Comment on the morphology of the erythrocytes.
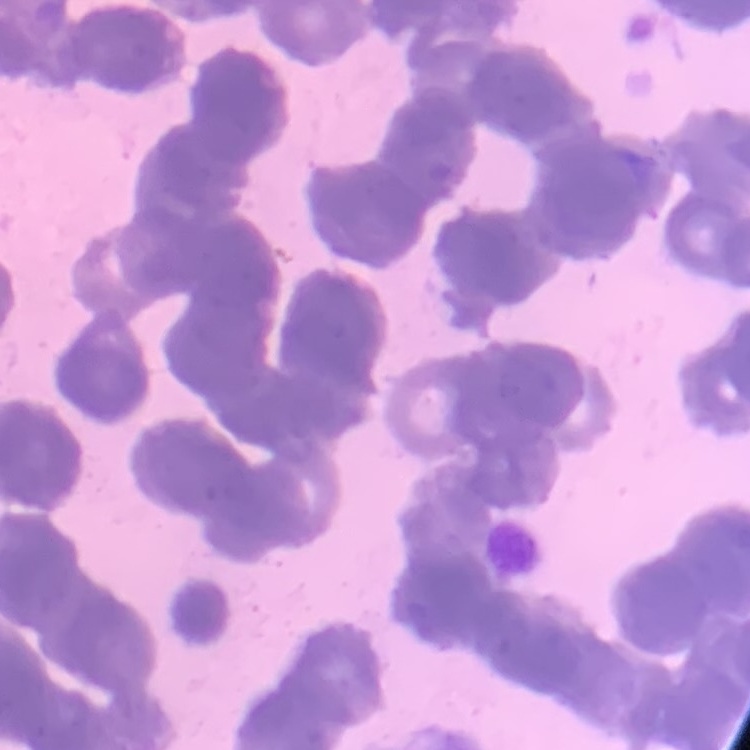

They show rouleaux formation.

Thin blood smear. Square crop of a larger photomicrograph. Stained with either Field's or Giemsa.